Report the malaria status of this cell.
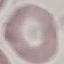

Uninfected.

Summary:
  - Capture: smartphone camera at the microscope eyepiece
  - Image type: automatically extracted cell patch, resized to 64 × 64 pixels
  - Stain: Giemsa
  - Preparation: thin smear